Report the malaria status of this cell.
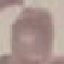

It is uninfected.

Giemsa stain. Automatically extracted cell patch, resized to 64 × 64 pixels. Photographed with a smartphone camera at the microscope eyepiece. Thin blood smear.